Outline each uninfected red blood cell.
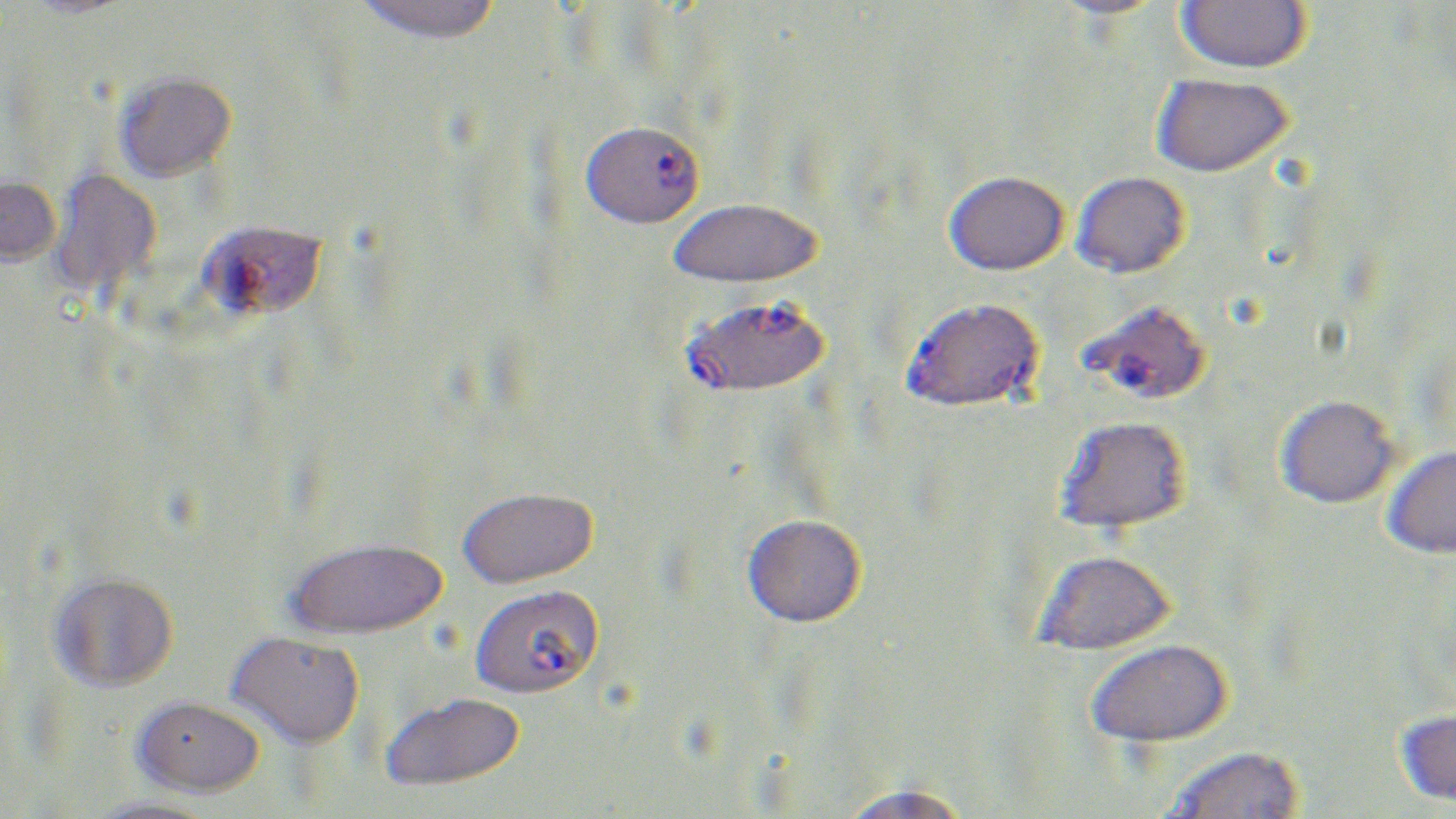
Approximate bounding boxes as [x1, y1, x2, y2] in pixels.
Uninfected red blood cells: [18, 0, 140, 19], [1045, 0, 1171, 20], [1176, 0, 1311, 73], [352, 1, 503, 45], [114, 71, 237, 182], [1151, 73, 1293, 177], [48, 168, 163, 300], [944, 170, 1068, 275], [1071, 171, 1190, 278], [0, 175, 62, 266], [667, 197, 823, 288], [1276, 395, 1399, 509], [1054, 415, 1192, 535], [1381, 445, 1456, 559], [457, 486, 598, 588], [742, 513, 866, 627], [286, 537, 446, 639], [1034, 549, 1176, 655], [49, 571, 179, 693], [227, 631, 365, 749], [1086, 639, 1233, 749], [379, 690, 525, 790], [132, 695, 265, 797], [1394, 710, 1456, 807], [1163, 745, 1304, 819], [836, 784, 972, 819], [83, 797, 221, 819].

slide-level diagnosis = Plasmodium falciparum
field of view = single
magnification = 1000x
preparation = thin blood film
Plasmodium falciparum-infected red blood cell locations = approximate bounding boxes as [x1, y1, x2, y2] in pixels: [580, 119, 706, 228], [197, 219, 328, 321], [900, 301, 1035, 410], [680, 302, 841, 399], [1086, 304, 1207, 403], [468, 584, 603, 699]
image size = 1456×819 pixels
modality = light microscopy
stain = May-Grünwald-Giemsa